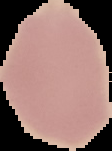 The area outside the segmented cell region is set to black. Malaria status: uninfected. Image is 112×151 pixels. From a thin blood film.